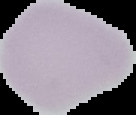

{
  "image_type": "segmented cell region with the area outside set to black",
  "image_size": "136×115 pixels",
  "preparation": "thin blood film",
  "malaria_status": "uninfected"
}